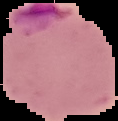

image size = 118×121 pixels
malaria status = parasitized
image type = segmented cell region on a black background
preparation = thin blood smear